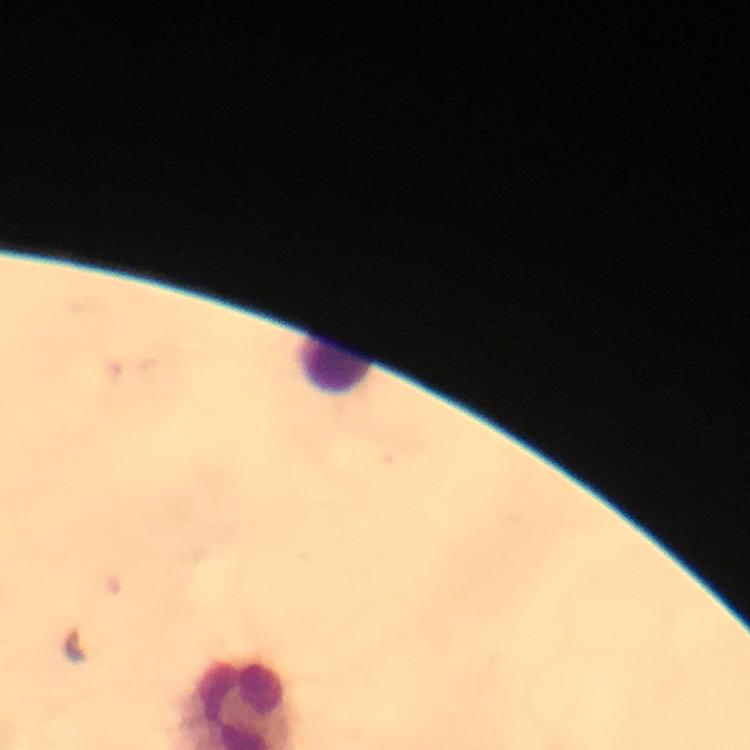

Approximate centers as [x, y] in pixels. Leukocyte locations: [336, 364]. Plasmodium parasites: none seen. From a diagnostic examination for malaria. Cropped region of a single field of view. Immersion oil was used. Smartphone photograph taken through a microscope. Image is 750×750 pixels. 100x magnification. Giemsa stain. Thick blood smear.